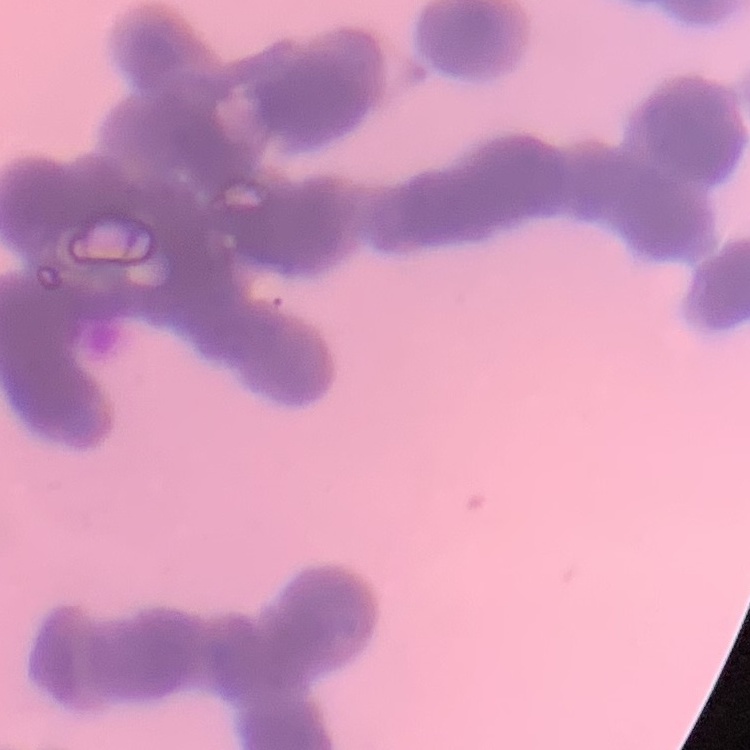
The erythrocytes exhibit rouleaux formation. One tile cut from a larger photomicrograph. Thin blood film. Stained with either Field's or Giemsa.